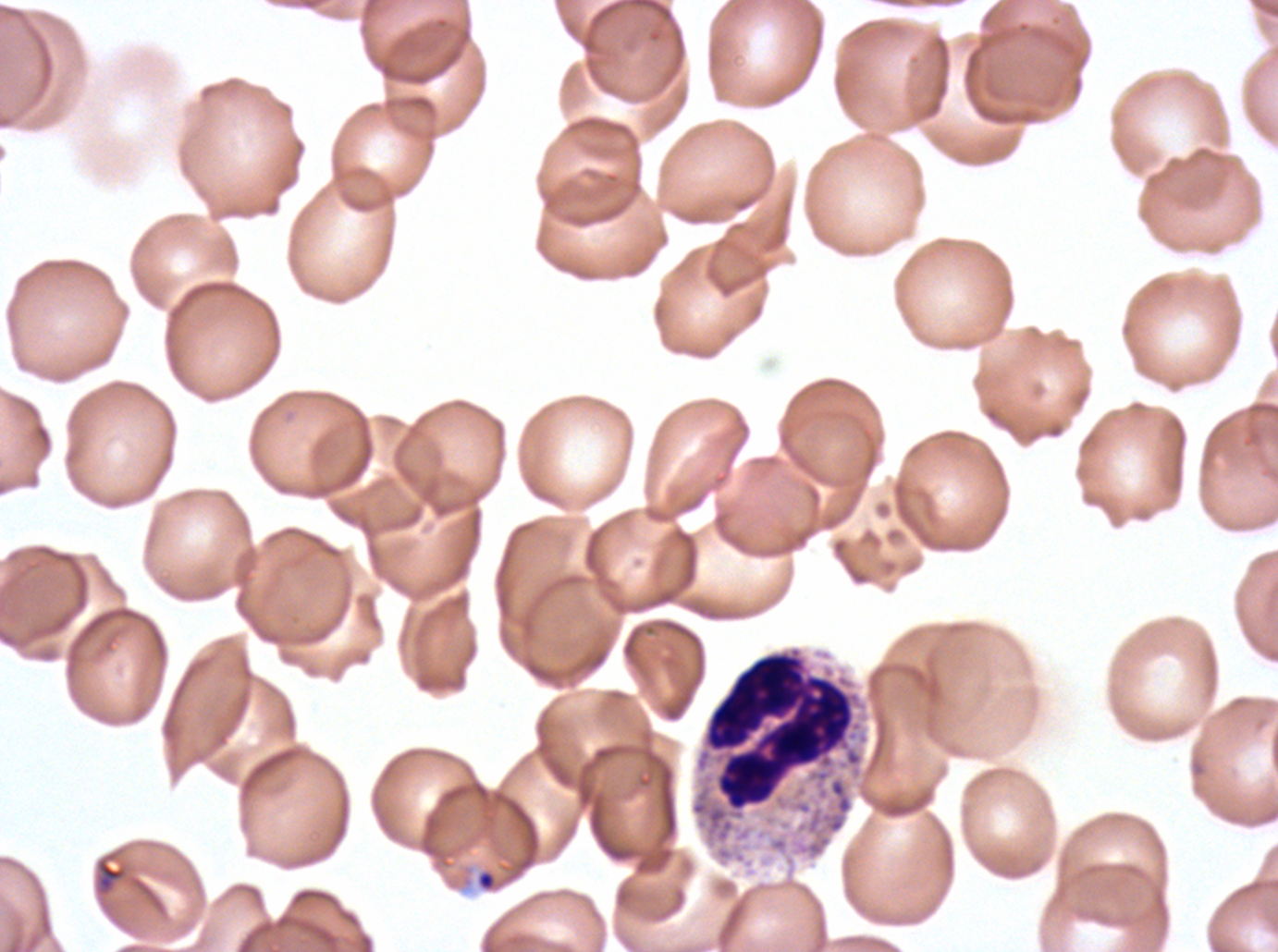
{
  "specimen": "P. falciparum cultured ex vivo for 24 to 48 hours, from a patient in The Gambia",
  "late_ring_early_trophozoite_locations": "approximate bounding boxes as {x1, y1, x2, y2} in pixels: {475, 869, 498, 892}",
  "preparation": "thin blood smear",
  "image_size": "1278×952 pixels",
  "field_of_view": "sub-image separated from a larger composite",
  "stain": "Giemsa",
  "leukocyte_locations": "approximate bounding boxes as {x1, y1, x2, y2} in pixels: {702, 646, 863, 812}"
}